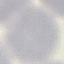
malaria_status: uninfected
preparation: thin blood smear
stain: Giemsa
image_type: cell patch, automatically extracted from a larger field of view and resized to 64 × 64 pixels
capture: smartphone camera at the microscope eyepiece